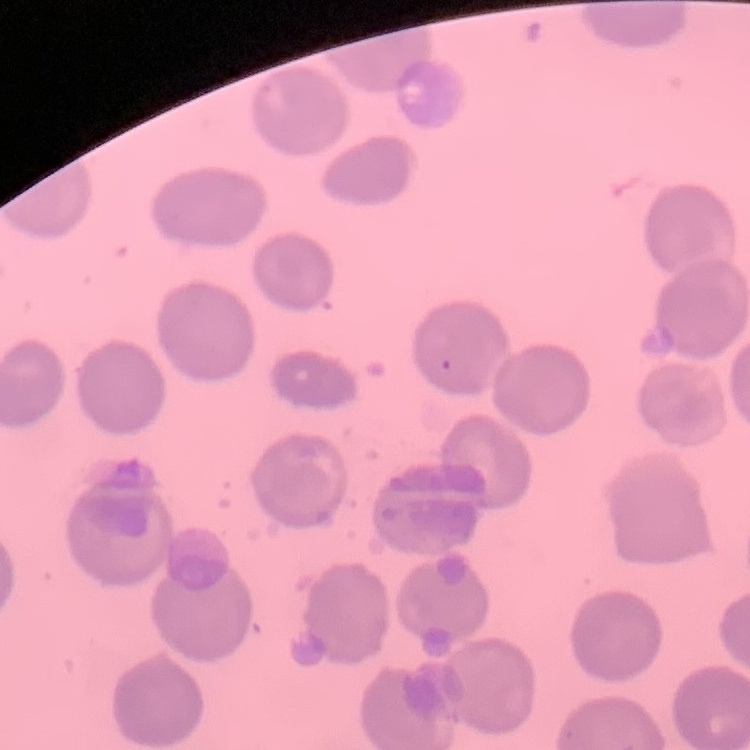

The erythrocytes exhibit no rouleaux formation. Square crop of a larger photomicrograph. Thin blood film. Stained with either Field's or Giemsa.